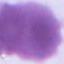
identification: erythrocyte
magnification: 1000x
modality: micrograph